Classify this cell by malaria status.
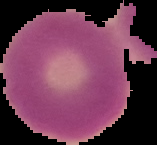

Uninfected.

preparation: thin blood film
image_size: 157×145 pixels
image_type: segmented cell region with the area outside set to black